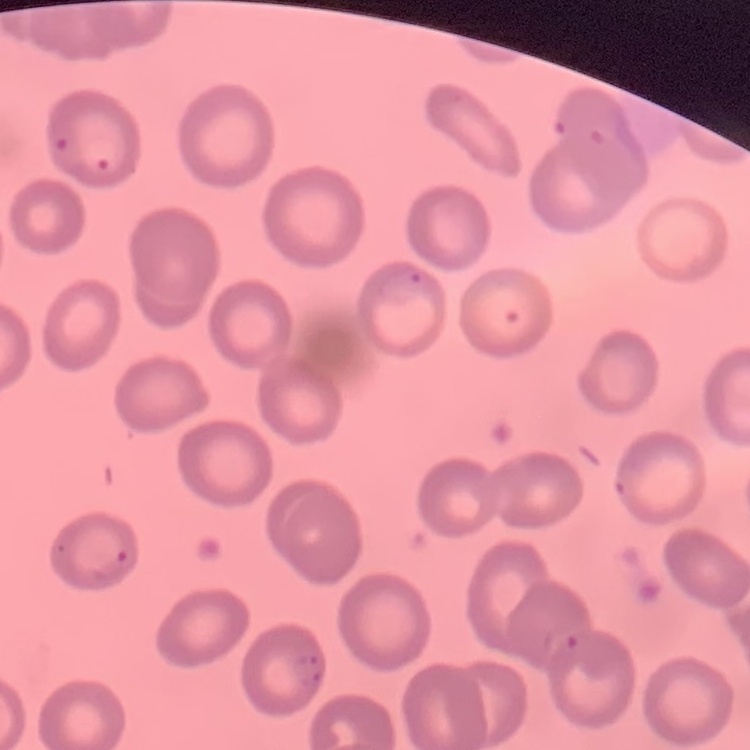
erythrocyte morphology = no rouleaux formation
stain = Field's or Giemsa
image type = one tile cut from a larger photomicrograph
preparation = thin blood smear